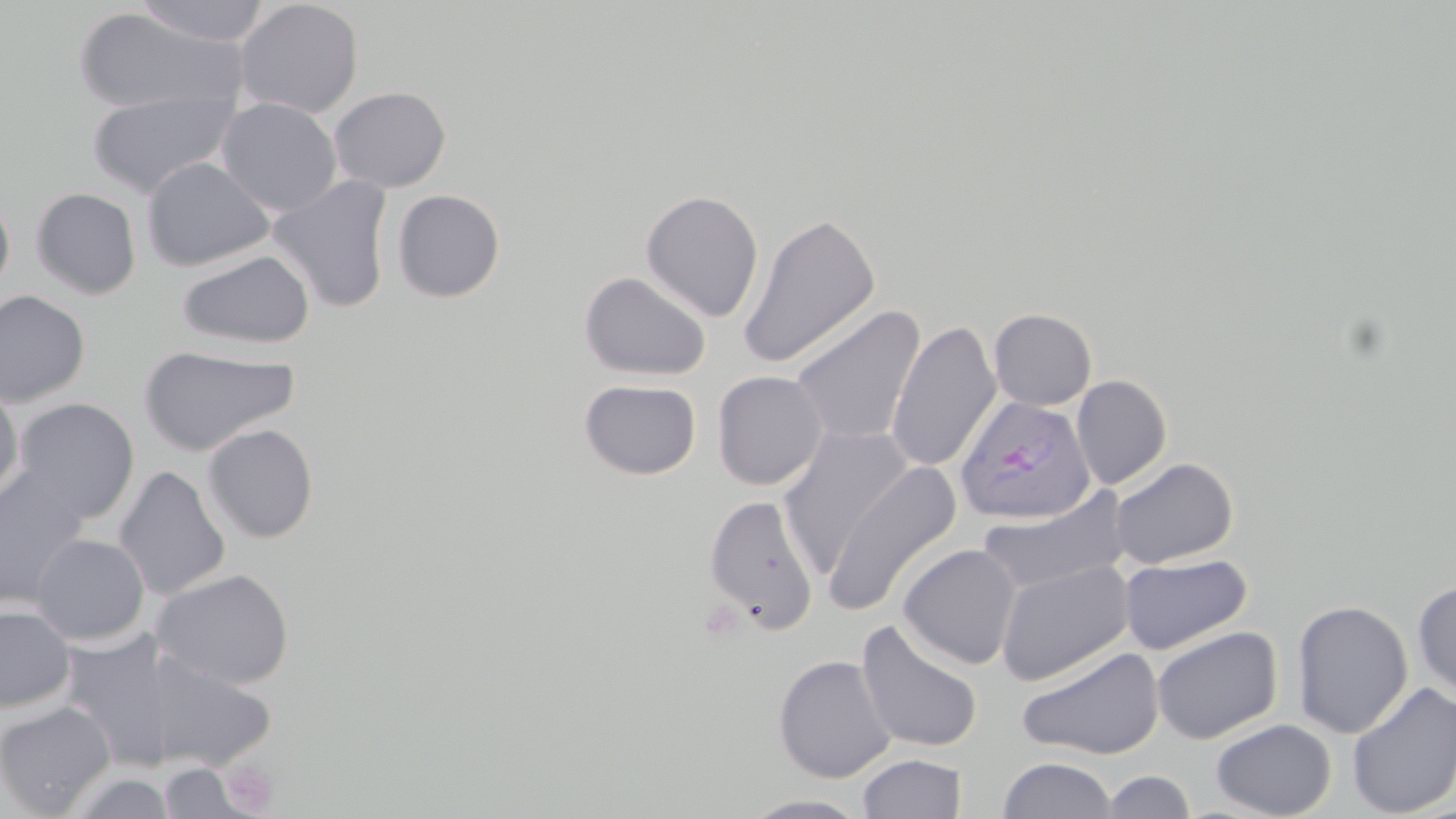
Summary:
  - Coordinate format: approximate bounding boxes as (x1, y1, x2, y2) in pixels
  - Plasmodium ovale-infected red blood cell locations: (954, 395, 1096, 525)
  - Platelet locations: (222, 760, 279, 815)
  - Uninfected red blood cell locations: (132, 0, 272, 47), (233, 0, 364, 118), (72, 7, 246, 116), (329, 86, 451, 193), (85, 89, 242, 197), (216, 97, 342, 216), (141, 157, 275, 271), (267, 174, 395, 313), (31, 187, 142, 300), (391, 189, 506, 303), (640, 190, 764, 323), (0, 192, 15, 299), (738, 211, 879, 369), (176, 249, 316, 350), (578, 271, 711, 381), (0, 290, 91, 408), (790, 304, 926, 447), (989, 308, 1097, 410), (887, 320, 1002, 472), (137, 344, 298, 457), (712, 370, 828, 490), (1071, 374, 1173, 490), (579, 379, 701, 480), (0, 382, 25, 503), (12, 398, 140, 524), (202, 423, 319, 544), (778, 428, 912, 577), (1108, 456, 1239, 569), (822, 461, 961, 617), (114, 466, 231, 600), (0, 469, 92, 609), (979, 486, 1132, 595), (704, 494, 819, 634), (30, 533, 149, 646), (898, 543, 1022, 669), (1119, 553, 1253, 655), (995, 559, 1134, 686), (151, 568, 295, 690), (1412, 578, 1456, 700), (1291, 599, 1413, 739), (0, 606, 76, 712), (856, 619, 984, 754), (1150, 625, 1283, 744), (59, 629, 177, 770), (1015, 645, 1165, 760), (142, 647, 277, 772), (773, 654, 897, 783), (1347, 681, 1456, 818), (0, 700, 117, 817), (1210, 718, 1337, 819), (857, 753, 968, 818), (997, 756, 1118, 818), (158, 763, 254, 818), (1102, 770, 1196, 818), (66, 771, 179, 818), (740, 794, 874, 818)
  - Slide-level diagnosis: Plasmodium ovale
  - Preparation: thin blood film
  - Magnification: 1000x
  - Image size: 1456×819 pixels
  - Modality: optical microscopy
  - Field of view: single
  - Stain: May-Grünwald-Giemsa